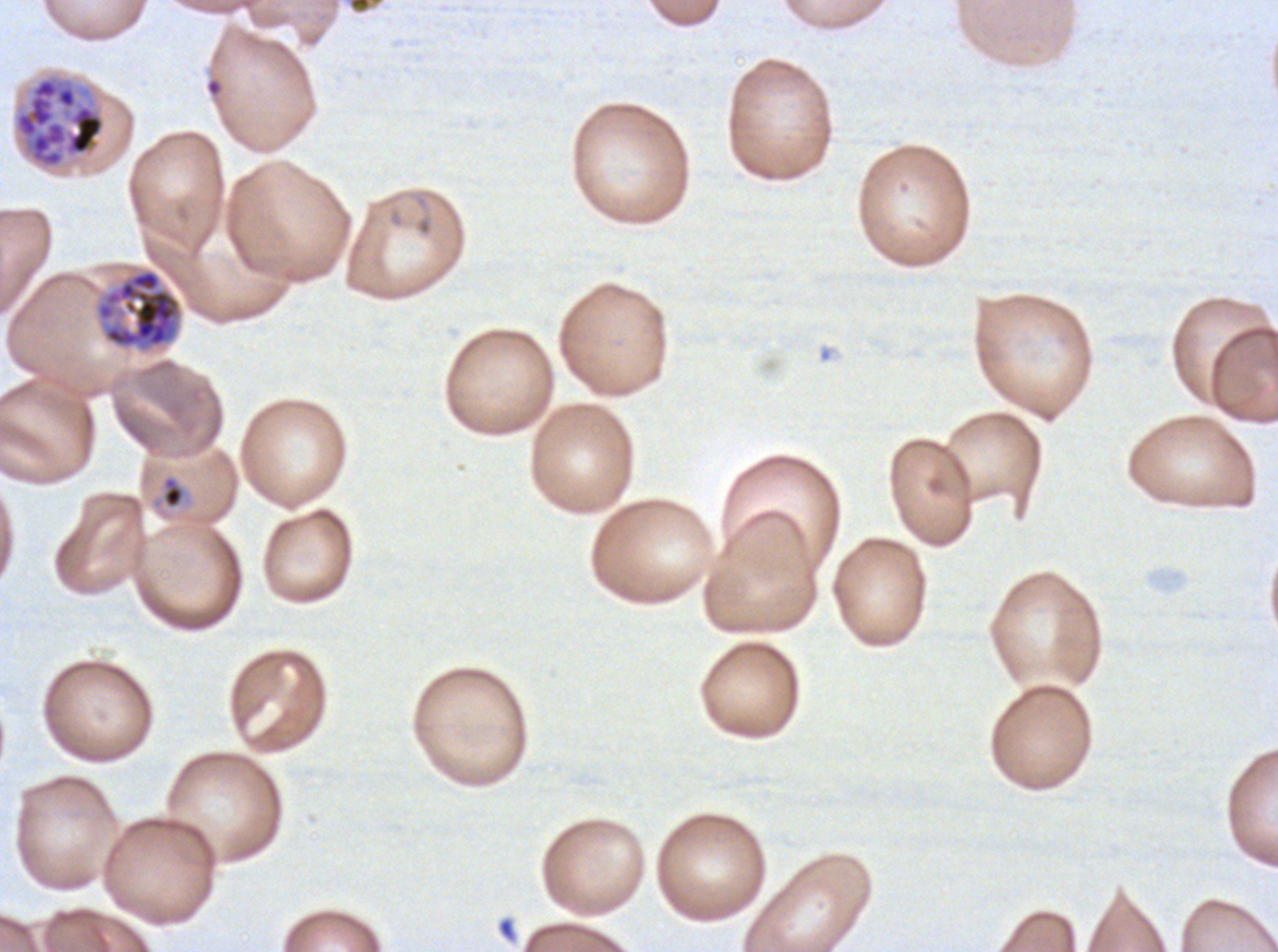

notation = approximate bounding rectangles given as corner coordinates in pixels from the top-left
late schizont locations = (x1=13, y1=74, x2=106, y2=170), (x1=94, y1=267, x2=183, y2=353)
late-ring/early-trophozoite locations = (x1=162, y1=477, x2=184, y2=508)
specimen = Plasmodium falciparum cultured ex vivo for 24 to 48 hours, from a patient in The Gambia
life-cycle stages observed = late-ring/early-trophozoite, late schizont
image size = 1278×952 pixels
preparation = thin blood film
field of view = one sub-image of a larger composite
stain = Giemsa